Report the malaria status.
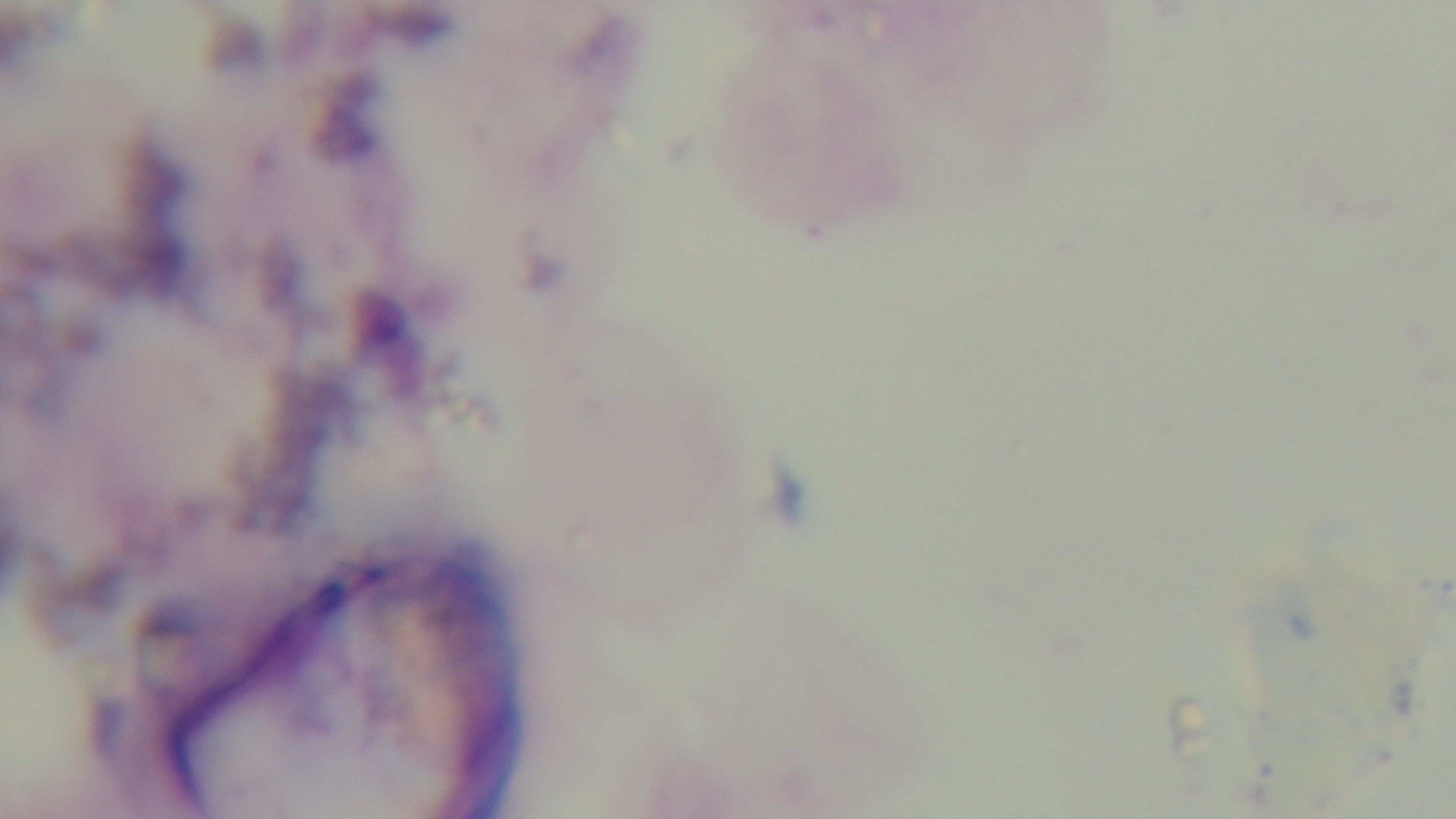
It is uninfected.

preparation: thick blood film
modality: light microscopy
objective: 100x oil immersion
field_of_view: single
capture: mounted 4K digital camera
stain: Giemsa